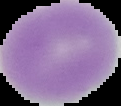
Image is 121×106 pixels. Malaria status: uninfected. The area outside the segmented cell region is set to black. From a thin blood film.